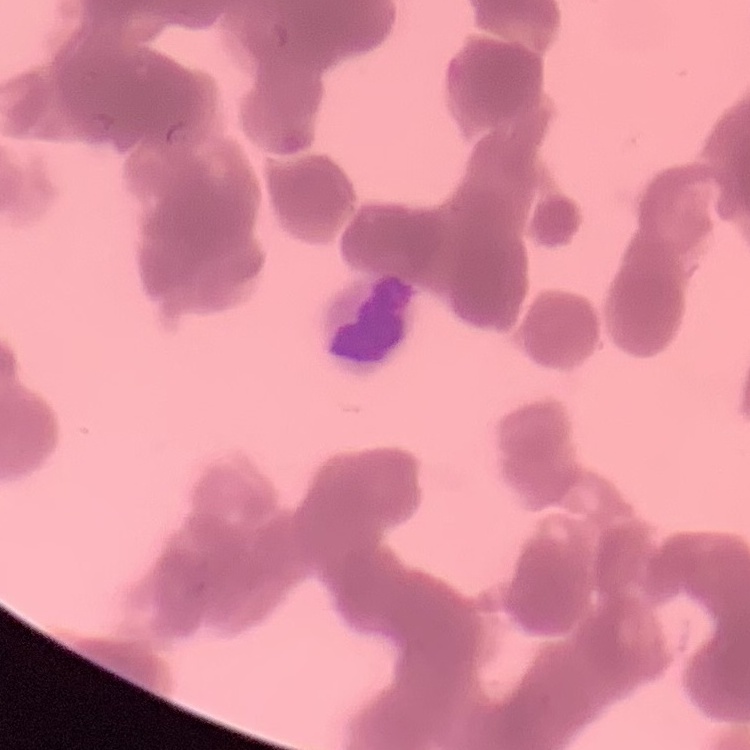
The erythrocytes exhibit rouleaux formation. One tile cut from a larger photomicrograph. Field's or Giemsa stain. Thin blood film.